Report the malaria status of this cell.
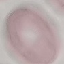
It is uninfected.

Summary:
  - Preparation: thin smear
  - Stain: Giemsa
  - Image type: cell patch, automatically extracted from a larger field of view and resized to 64 × 64 pixels
  - Capture: smartphone camera at the microscope eyepiece